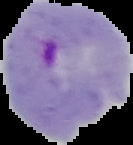
image_type: segmented cell region on a black background
malaria_status: parasitized
image_size: 133×145 pixels
preparation: thin blood film